Assess this cell for malaria.
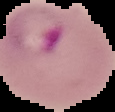
Parasitized.

image type = segmented cell region with the area outside set to black
image size = 115×112 pixels
preparation = thin blood smear